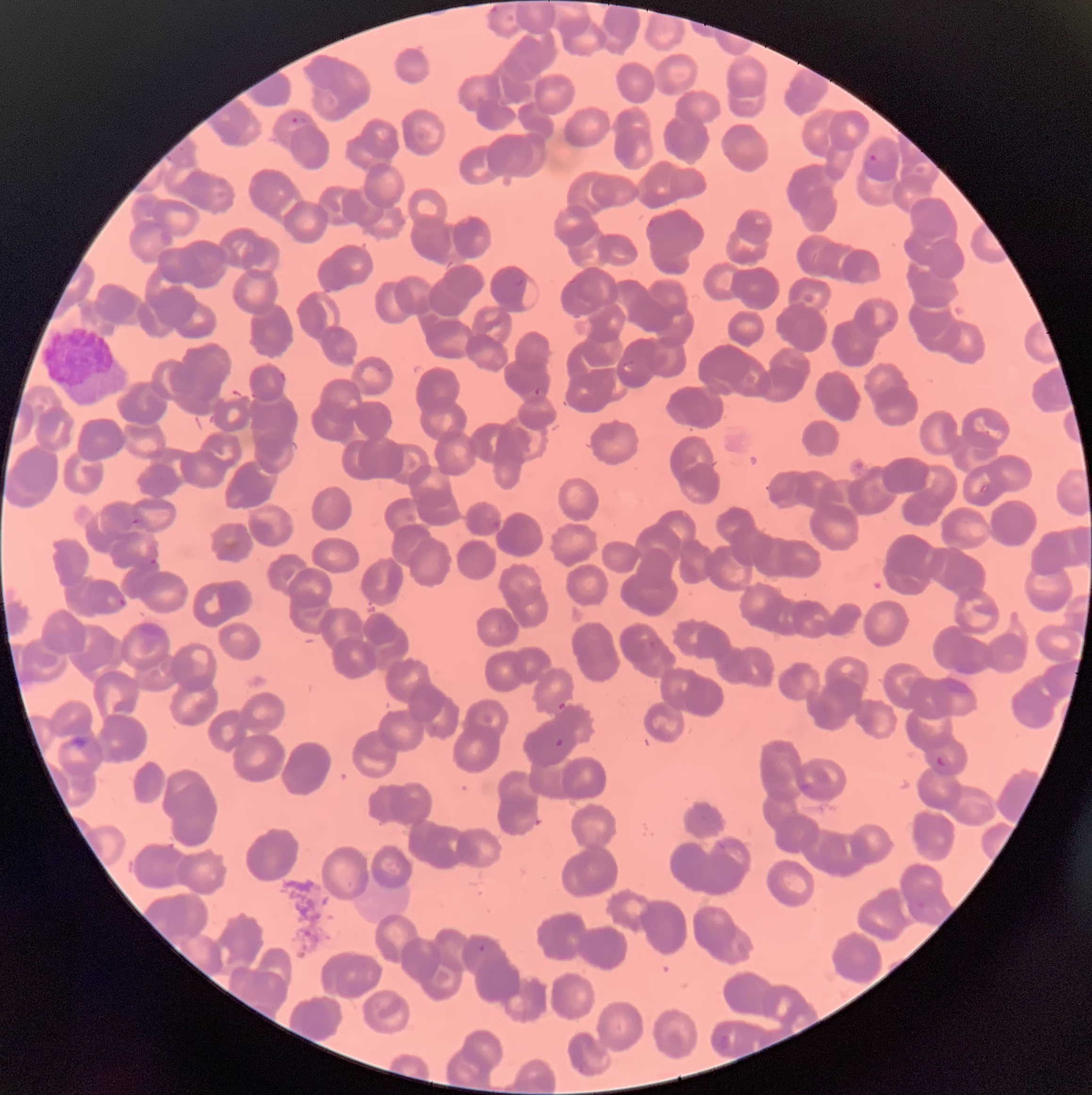

Summary:
  - Coordinate format: approximate bounding boxes as (x1,y1)-(x2,y2) corner pairs in pixels
  - Plasmodium parasite locations: (290,114)-(307,127), (864,151)-(884,173), (514,276)-(523,287), (621,360)-(635,373), (220,386)-(248,406), (533,386)-(543,397), (130,516)-(143,527), (149,557)-(158,567), (117,595)-(127,608), (554,737)-(566,749), (936,755)-(946,767), (477,943)-(486,953), (719,1033)-(731,1049)
  - Red blood cell morphology: rouleaux formation
  - Preparation: thin blood film
  - Modality: optical microscopy
  - Image size: 1092×1095 pixels